Assess this cell for malaria.
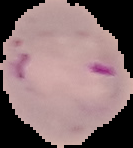
Parasitized.

Summary:
  - Image size: 133×148 pixels
  - Image type: cell region segmented out of the field of view; surrounding area masked to black
  - Preparation: thin blood smear